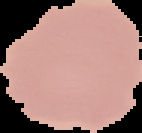
image_size: 142×133 pixels
image_type: segmented cell region on a black background
malaria_status: uninfected
preparation: thin blood smear